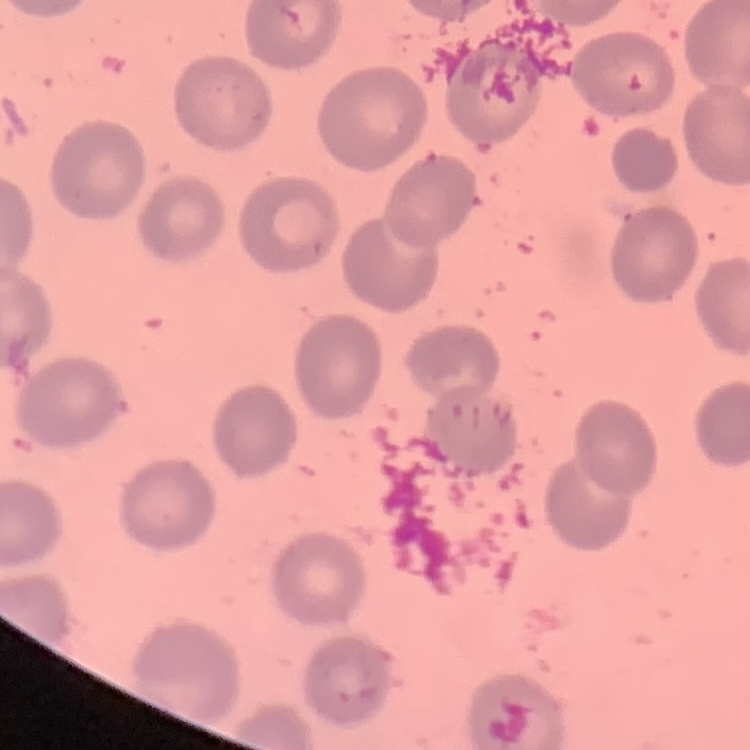 The erythrocytes exhibit no rouleaux formation. Field's or Giemsa stain. One tile cut from a larger photomicrograph. Thin blood film.